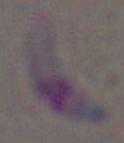

Summary:
  - Modality: photomicrograph
  - Magnification: 1000x
  - Identification: Toxoplasma gondii